Find each parasitized red blood cell.
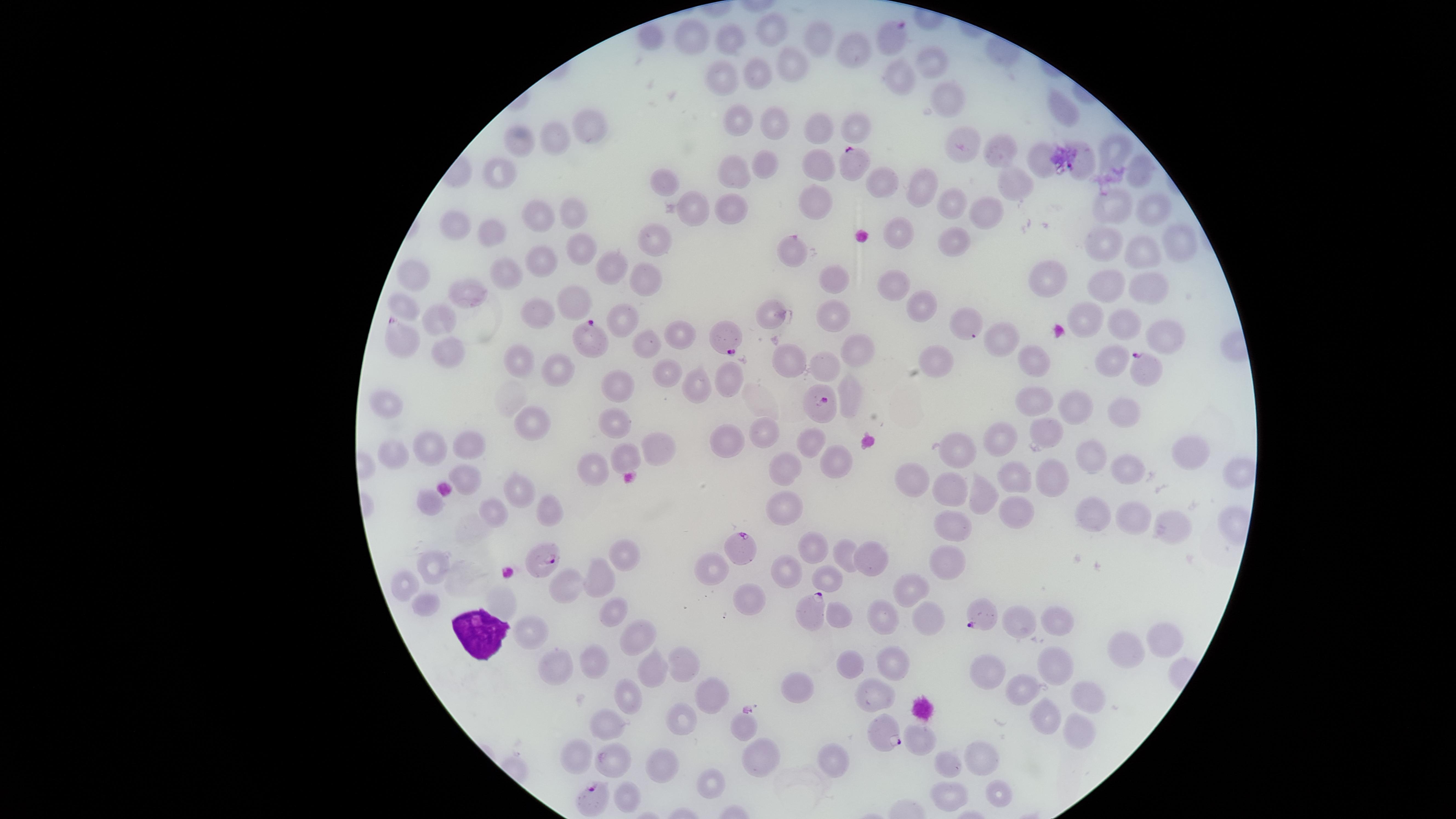

Approximate marker points as (x, y) in pixels.
Parasitized red blood cells: (891, 35), (851, 168), (724, 338), (587, 339), (396, 341), (1141, 366), (820, 400), (739, 546), (541, 564), (809, 614), (985, 614), (888, 736), (594, 796).

Approximate marker points as (x, y) in pixels.
Summary:
  - White blood cells: (483, 635)
  - Uninfected red blood cells: (770, 30), (690, 35), (817, 36), (732, 42), (857, 50), (792, 59), (935, 59), (756, 68), (898, 75), (721, 78), (948, 100), (1060, 107), (735, 117), (775, 122), (593, 123), (856, 123), (824, 127), (561, 136), (520, 141), (959, 146), (1113, 148), (1003, 151), (1037, 160), (1082, 163), (770, 165), (501, 170), (735, 171), (819, 171), (1140, 171), (666, 181), (884, 184), (922, 184), (1013, 185), (949, 202), (815, 203), (727, 205), (1113, 208), (1151, 209), (987, 210), (692, 211), (570, 213), (536, 218), (457, 223), (898, 232), (491, 234), (655, 241), (951, 241), (1106, 242), (1181, 242), (797, 249), (580, 251), (1140, 253), (547, 260), (606, 269), (1052, 272), (504, 273), (415, 275), (832, 277), (645, 281), (892, 285), (1102, 285), (1143, 286), (472, 296), (572, 306), (922, 306), (407, 311), (1085, 315), (536, 317), (774, 317), (961, 321), (626, 322), (832, 322), (1117, 325), (439, 326), (681, 335), (1159, 335), (1001, 338), (446, 346), (641, 350), (858, 350), (938, 355), (1033, 358), (788, 360), (1110, 361), (516, 362), (820, 364), (554, 371), (663, 373), (733, 376), (619, 383), (698, 384), (849, 394), (386, 400), (1031, 400), (1074, 402), (1118, 411), (534, 422), (616, 425), (1045, 427), (763, 432), (1009, 434), (812, 442), (726, 443), (432, 447), (654, 447), (959, 447), (469, 449), (392, 454), (1187, 455), (622, 456), (1094, 456), (831, 463), (592, 467), (1127, 467), (783, 471), (1233, 472), (466, 475), (910, 476), (1018, 476), (1051, 479), (953, 483), (516, 491), (982, 493), (546, 507), (785, 507), (428, 508), (495, 510), (1013, 514), (1090, 515), (1126, 518), (1171, 524), (955, 525), (815, 546), (845, 553), (620, 554), (867, 557), (946, 559), (432, 560), (714, 564), (787, 572), (601, 575), (825, 577), (406, 586), (567, 589), (912, 590), (745, 598), (500, 601), (428, 604), (613, 614), (841, 615), (886, 619), (930, 622), (1017, 622), (1055, 623), (531, 627), (637, 637), (1161, 640), (1121, 655), (889, 661), (592, 663), (684, 664), (851, 667), (1054, 667), (556, 669), (651, 670), (989, 671), (796, 687), (705, 692), (1023, 694), (629, 696), (870, 701), (1087, 702), (1045, 717), (682, 718), (744, 728), (605, 730), (1076, 730), (918, 739), (981, 751), (578, 753), (612, 756), (835, 760), (664, 762), (758, 762), (948, 764), (710, 782), (946, 792), (997, 792)
  - Visible region: circular
  - Field of view: single
  - Image size: 1456×819 pixels
  - Stain: Giemsa
  - Preparation: thin blood film
  - Capture: smartphone photograph through the microscope eyepiece
  - Species: Plasmodium falciparum